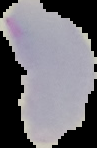
malaria status = uninfected
image size = 97×148 pixels
image type = segmented cell region on a black background
preparation = thin blood film